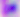

Captured at 400x magnification. Micrograph. Toxoplasma gondii is seen.